Assess this cell for malaria.
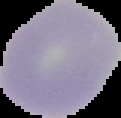

Uninfected.

Segmented cell region on a black background. Image is 121×118 pixels. From a thin blood film.